Name the cell type shown.
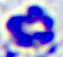

A leukocyte.

Photomicrograph. Captured at 400x magnification.